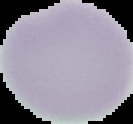
Summary:
  - Preparation: thin blood film
  - Malaria status: uninfected
  - Image type: segmented cell region with the area outside set to black
  - Image size: 133×124 pixels